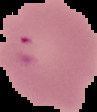 Result: malaria parasites detected. Cell region segmented out of the field of view; the surrounding area is masked to black. Image is 97×112 pixels. From a thin blood smear.